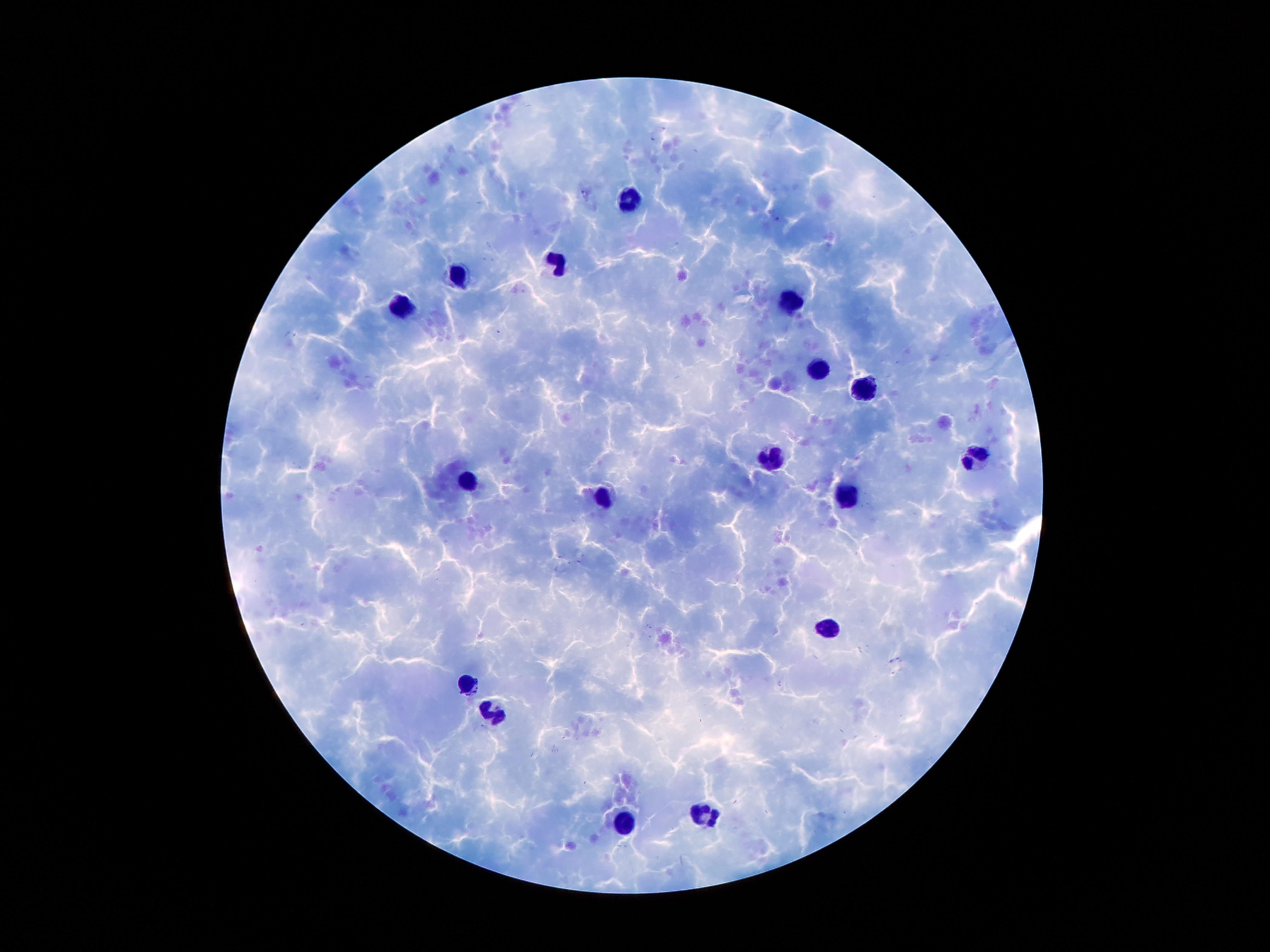
Approximate centers as (x, y) in pixels.
Summary:
  - Leukocyte locations: (631, 200), (563, 260), (463, 276), (793, 302), (407, 305), (820, 368), (865, 390), (973, 456), (770, 459), (469, 481), (846, 496), (608, 498), (828, 628), (468, 683), (491, 710), (705, 811), (628, 822)
  - Stain: Giemsa
  - Patient malaria status: positive for Plasmodium falciparum
  - Capture: smartphone through the microscope eyepiece
  - Magnification: 100x
  - Preparation: thick blood film
  - Image size: 1270×952 pixels
  - Malaria parasites: not detected
  - Field of view: one from this slide